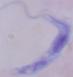

Photomicrograph. A trypanosome is seen. 1000x magnification.